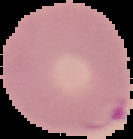

Image is 133×139 pixels. Malaria status: parasitized. From a thin blood smear. The area outside the segmented cell region is set to black.